Report the malaria status of this cell.
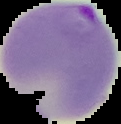
Parasitized.

{
  "image_size": "121×124 pixels",
  "preparation": "thin blood smear",
  "image_type": "segmented cell region on a black background"
}